Report the malaria status of this cell.
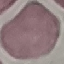
It is uninfected.

Summary:
  - Preparation: thin blood film
  - Stain: Giemsa
  - Capture: smartphone camera at the microscope eyepiece
  - Image type: automatically extracted cell patch, resized to 64 × 64 pixels